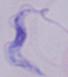

identification: trypanosome
modality: micrograph
magnification: 1000x